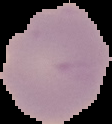

malaria_status: uninfected
preparation: thin blood film
image_type: cell region segmented out of the field of view; surrounding area masked to black
image_size: 112×124 pixels